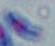

identification = Toxoplasma gondii
modality = photomicrograph
magnification = 1000x